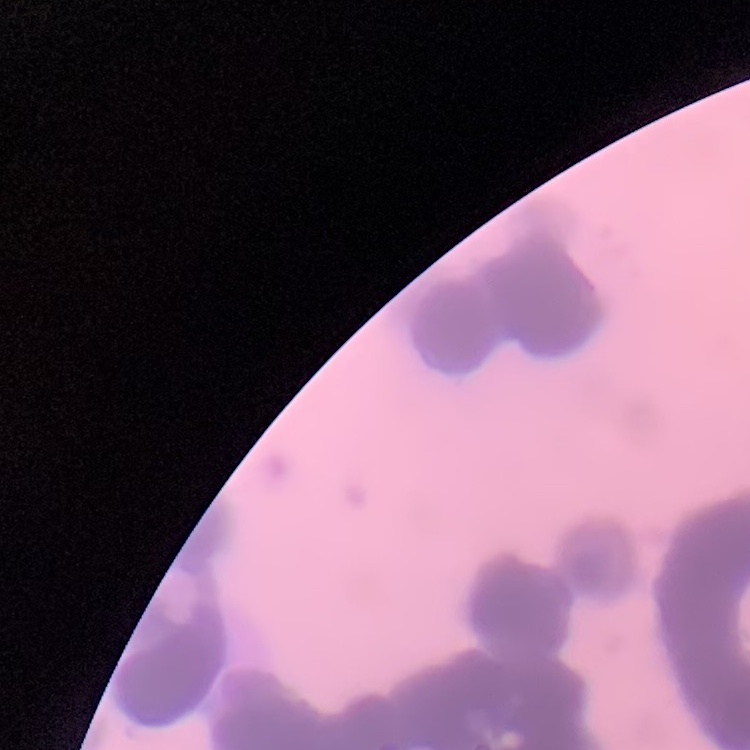

red_blood_cell_morphology: rouleaux formation
preparation: thin blood smear
image_type: one tile cut from a larger photomicrograph
stain: Field's or Giemsa